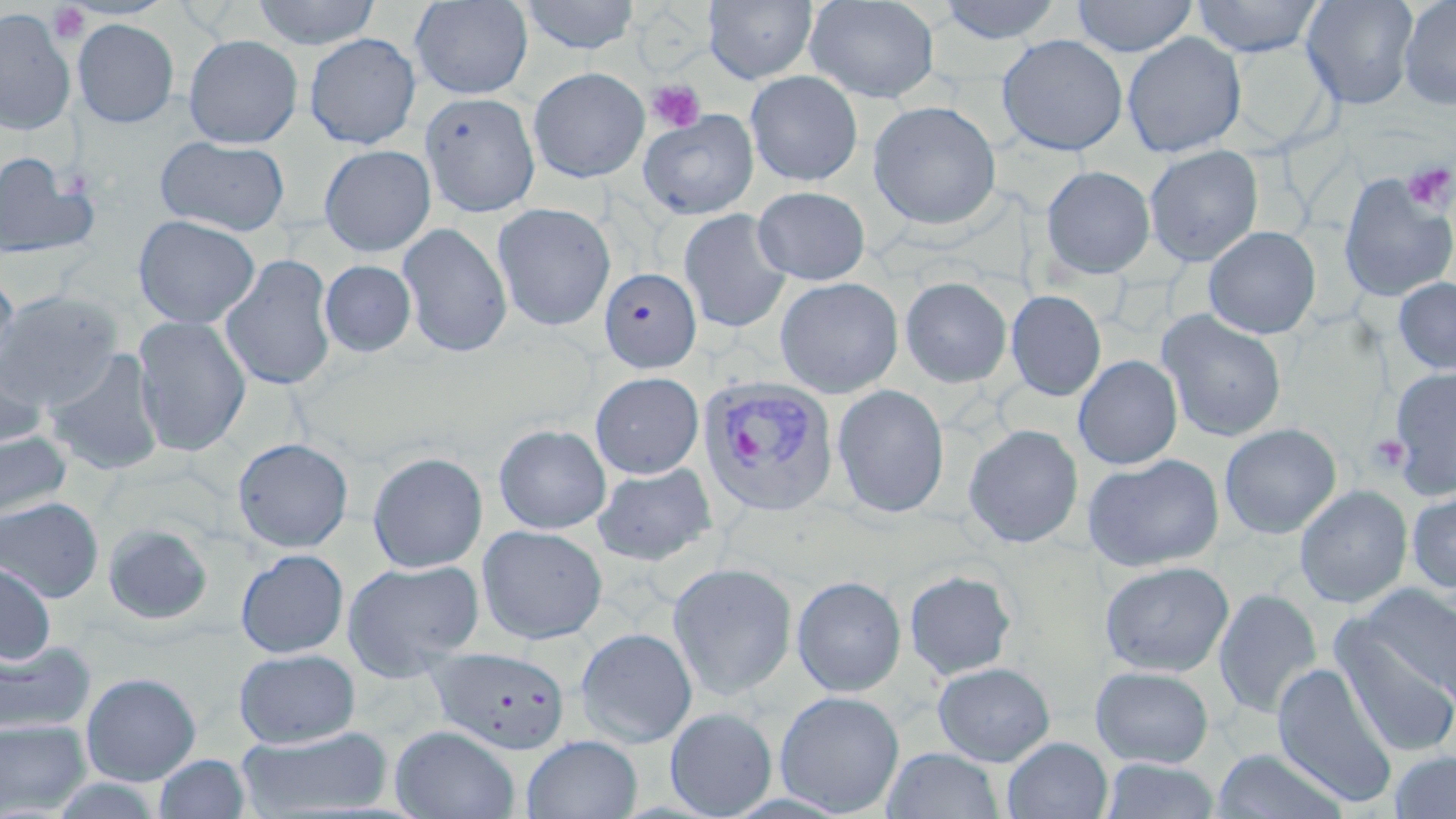

Summary:
  - Coordinate format: approximate bounding boxes as named x1/y1/x2/y2 corners in pixels
  - Plasmodium vivax-infected red blood cell locations: (x1=697, y1=377, x2=840, y2=518)
  - Uninfected red blood cell locations: (x1=251, y1=0, x2=382, y2=49), (x1=409, y1=0, x2=533, y2=99), (x1=519, y1=0, x2=641, y2=54), (x1=703, y1=0, x2=818, y2=84), (x1=804, y1=0, x2=940, y2=103), (x1=1071, y1=0, x2=1198, y2=57), (x1=1191, y1=0, x2=1324, y2=57), (x1=1301, y1=0, x2=1419, y2=109), (x1=1398, y1=0, x2=1456, y2=111), (x1=935, y1=1, x2=1064, y2=44), (x1=0, y1=8, x2=76, y2=135), (x1=72, y1=18, x2=179, y2=128), (x1=1122, y1=32, x2=1246, y2=158), (x1=303, y1=33, x2=422, y2=149), (x1=183, y1=34, x2=303, y2=147), (x1=996, y1=34, x2=1128, y2=156), (x1=1226, y1=42, x2=1336, y2=149), (x1=528, y1=67, x2=650, y2=182), (x1=745, y1=71, x2=863, y2=186), (x1=419, y1=92, x2=540, y2=217), (x1=867, y1=100, x2=1002, y2=230), (x1=638, y1=109, x2=760, y2=220), (x1=155, y1=135, x2=291, y2=236), (x1=319, y1=144, x2=436, y2=256), (x1=1144, y1=145, x2=1264, y2=266), (x1=0, y1=149, x2=100, y2=262), (x1=1041, y1=165, x2=1155, y2=278), (x1=1338, y1=173, x2=1455, y2=304), (x1=752, y1=186, x2=871, y2=284), (x1=492, y1=202, x2=616, y2=331), (x1=678, y1=209, x2=792, y2=333), (x1=133, y1=214, x2=261, y2=328), (x1=398, y1=222, x2=512, y2=358), (x1=1204, y1=226, x2=1321, y2=339), (x1=221, y1=253, x2=337, y2=391), (x1=319, y1=260, x2=417, y2=358), (x1=599, y1=266, x2=704, y2=373), (x1=0, y1=271, x2=20, y2=384), (x1=775, y1=277, x2=903, y2=398), (x1=900, y1=277, x2=1012, y2=387), (x1=1393, y1=277, x2=1456, y2=376), (x1=0, y1=290, x2=123, y2=409), (x1=1006, y1=290, x2=1106, y2=401), (x1=1156, y1=310, x2=1288, y2=443), (x1=133, y1=315, x2=251, y2=457), (x1=43, y1=349, x2=166, y2=476), (x1=0, y1=354, x2=50, y2=451), (x1=1073, y1=355, x2=1183, y2=469), (x1=1388, y1=367, x2=1456, y2=500), (x1=590, y1=372, x2=704, y2=478), (x1=832, y1=384, x2=949, y2=519), (x1=493, y1=423, x2=612, y2=534), (x1=1219, y1=423, x2=1341, y2=539), (x1=963, y1=424, x2=1084, y2=549), (x1=0, y1=429, x2=72, y2=523), (x1=232, y1=437, x2=354, y2=553), (x1=367, y1=451, x2=488, y2=573), (x1=1083, y1=453, x2=1224, y2=572), (x1=592, y1=463, x2=717, y2=566), (x1=1294, y1=484, x2=1413, y2=608), (x1=1405, y1=487, x2=1456, y2=595), (x1=0, y1=497, x2=104, y2=602), (x1=101, y1=523, x2=215, y2=627), (x1=477, y1=525, x2=608, y2=644), (x1=235, y1=549, x2=349, y2=658), (x1=342, y1=559, x2=483, y2=681), (x1=0, y1=560, x2=57, y2=665), (x1=1099, y1=560, x2=1235, y2=677), (x1=667, y1=562, x2=798, y2=700), (x1=904, y1=570, x2=1017, y2=680), (x1=791, y1=575, x2=907, y2=696), (x1=1359, y1=584, x2=1456, y2=710), (x1=1213, y1=588, x2=1322, y2=719), (x1=1333, y1=617, x2=1456, y2=758), (x1=575, y1=627, x2=697, y2=748), (x1=0, y1=639, x2=96, y2=738), (x1=429, y1=647, x2=570, y2=754), (x1=234, y1=648, x2=361, y2=748), (x1=932, y1=662, x2=1056, y2=765), (x1=1272, y1=662, x2=1399, y2=807), (x1=1091, y1=665, x2=1214, y2=767), (x1=81, y1=672, x2=202, y2=785), (x1=775, y1=690, x2=904, y2=816), (x1=665, y1=707, x2=777, y2=818), (x1=0, y1=719, x2=92, y2=816), (x1=390, y1=725, x2=520, y2=819), (x1=234, y1=727, x2=393, y2=817), (x1=522, y1=734, x2=643, y2=819), (x1=1002, y1=736, x2=1113, y2=819), (x1=883, y1=748, x2=1004, y2=819), (x1=1210, y1=748, x2=1351, y2=819), (x1=1387, y1=750, x2=1456, y2=818), (x1=153, y1=754, x2=251, y2=819), (x1=1101, y1=758, x2=1219, y2=819)
  - Platelet locations: (x1=48, y1=3, x2=92, y2=46), (x1=647, y1=79, x2=706, y2=133), (x1=1402, y1=162, x2=1455, y2=213), (x1=1367, y1=432, x2=1411, y2=475)
  - Slide-level diagnosis: Plasmodium vivax
  - Field of view: one of a larger specimen
  - Preparation: thin blood film
  - Stain: May-Grünwald-Giemsa
  - Modality: light microscopy
  - Magnification: 1000x
  - Image size: 1456×819 pixels